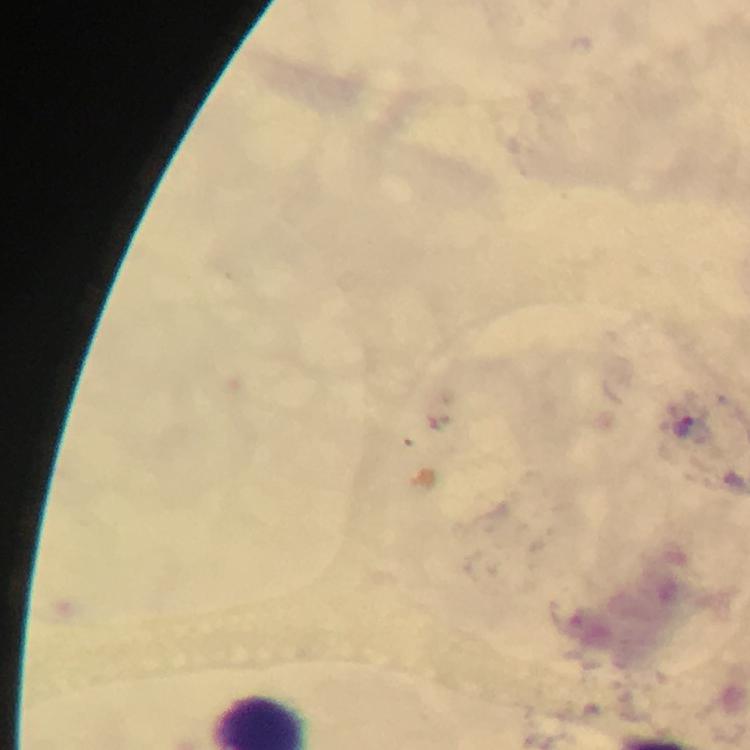
100x magnification. Immersion oil applied. Thick blood film. Cropped region of a single field of view. Smartphone photograph taken through a microscope. Image is 750×750 pixels. From a malaria diagnostic workup. Giemsa stain.